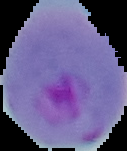
Summary:
  - Malaria status: parasitized
  - Preparation: thin blood smear
  - Image type: segmented cell region with the area outside set to black
  - Image size: 127×151 pixels